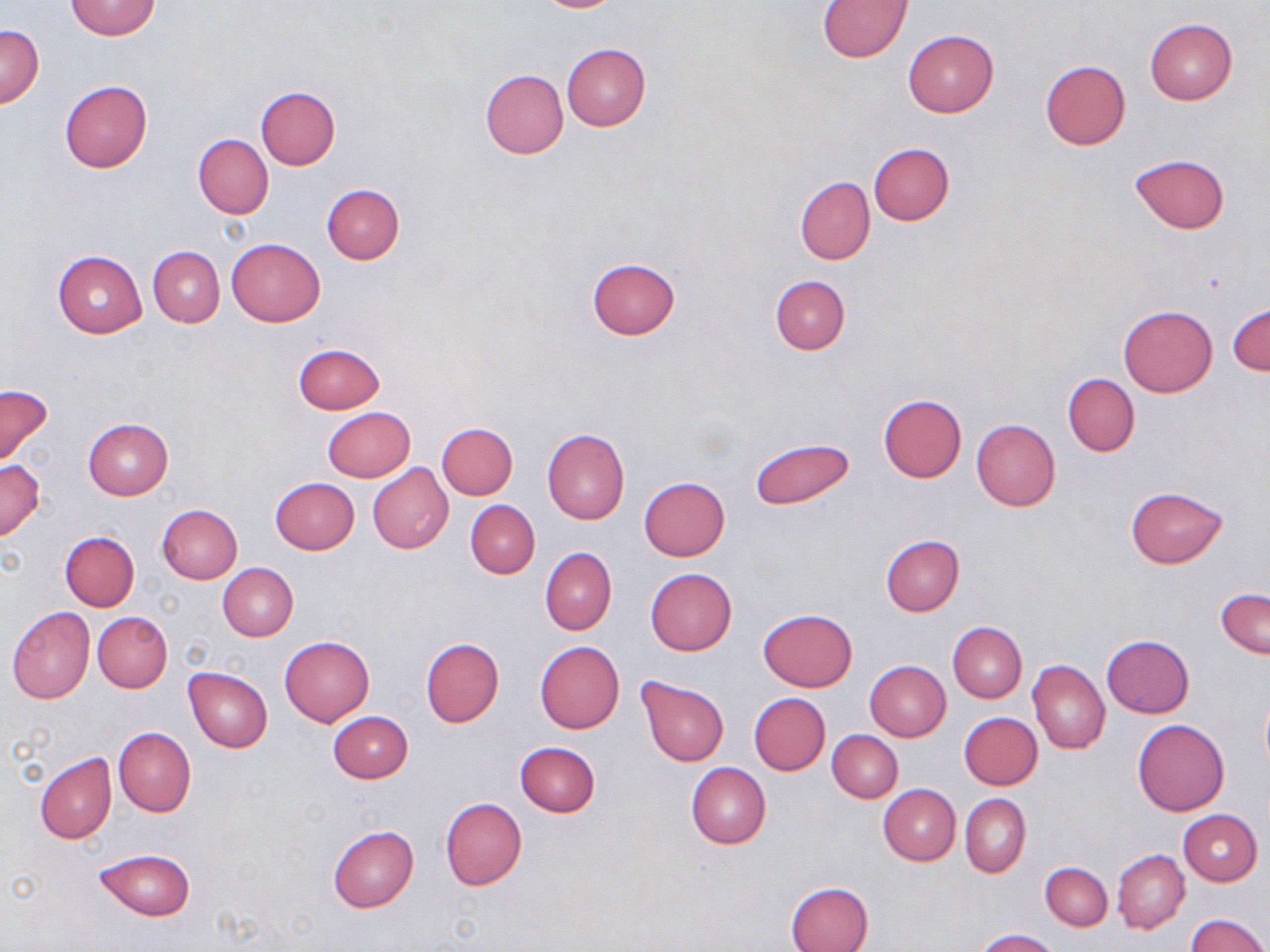
Summary:
  - Coordinate format: approximate bounding boxes as named x1/y1/x2/y2 corners in pixels
  - Uninfected red blood cell locations: (x1=534, y1=0, x2=624, y2=12), (x1=66, y1=1, x2=160, y2=40), (x1=818, y1=1, x2=911, y2=61), (x1=1145, y1=18, x2=1237, y2=105), (x1=0, y1=25, x2=44, y2=108), (x1=903, y1=30, x2=998, y2=117), (x1=561, y1=44, x2=651, y2=131), (x1=1039, y1=60, x2=1130, y2=150), (x1=480, y1=69, x2=568, y2=159), (x1=59, y1=81, x2=153, y2=171), (x1=256, y1=86, x2=340, y2=169), (x1=193, y1=134, x2=273, y2=218), (x1=867, y1=143, x2=954, y2=225), (x1=1130, y1=154, x2=1229, y2=235), (x1=795, y1=177, x2=874, y2=264), (x1=322, y1=184, x2=404, y2=263), (x1=227, y1=237, x2=325, y2=326), (x1=148, y1=246, x2=224, y2=327), (x1=52, y1=250, x2=146, y2=339), (x1=587, y1=257, x2=680, y2=339), (x1=770, y1=275, x2=850, y2=354), (x1=1228, y1=303, x2=1269, y2=375), (x1=1119, y1=305, x2=1217, y2=397), (x1=293, y1=343, x2=385, y2=413), (x1=1063, y1=374, x2=1139, y2=457), (x1=0, y1=384, x2=54, y2=469), (x1=878, y1=395, x2=967, y2=483), (x1=323, y1=407, x2=415, y2=482), (x1=83, y1=418, x2=172, y2=499), (x1=972, y1=420, x2=1061, y2=511), (x1=437, y1=422, x2=517, y2=500), (x1=542, y1=428, x2=630, y2=524), (x1=750, y1=438, x2=855, y2=509), (x1=0, y1=459, x2=45, y2=542), (x1=368, y1=464, x2=453, y2=554), (x1=270, y1=477, x2=359, y2=555), (x1=639, y1=477, x2=730, y2=560), (x1=1126, y1=487, x2=1228, y2=568), (x1=465, y1=499, x2=540, y2=578), (x1=156, y1=504, x2=242, y2=583), (x1=61, y1=531, x2=139, y2=611), (x1=881, y1=536, x2=964, y2=615), (x1=540, y1=548, x2=616, y2=634), (x1=218, y1=563, x2=297, y2=641), (x1=645, y1=568, x2=737, y2=655), (x1=1215, y1=587, x2=1270, y2=660), (x1=7, y1=607, x2=95, y2=704), (x1=759, y1=609, x2=857, y2=691), (x1=93, y1=612, x2=172, y2=692), (x1=947, y1=622, x2=1026, y2=702), (x1=1101, y1=635, x2=1193, y2=718), (x1=279, y1=636, x2=375, y2=727), (x1=421, y1=637, x2=505, y2=727), (x1=535, y1=640, x2=624, y2=733), (x1=1028, y1=659, x2=1110, y2=754), (x1=865, y1=661, x2=950, y2=742), (x1=183, y1=666, x2=273, y2=752), (x1=636, y1=677, x2=730, y2=767), (x1=1260, y1=691, x2=1270, y2=773), (x1=749, y1=692, x2=830, y2=776), (x1=328, y1=711, x2=413, y2=783), (x1=958, y1=713, x2=1043, y2=790), (x1=1132, y1=718, x2=1229, y2=816), (x1=113, y1=728, x2=196, y2=817), (x1=828, y1=729, x2=902, y2=802), (x1=515, y1=741, x2=600, y2=817), (x1=35, y1=753, x2=116, y2=843), (x1=686, y1=762, x2=771, y2=849), (x1=879, y1=785, x2=960, y2=865), (x1=960, y1=794, x2=1030, y2=876), (x1=439, y1=798, x2=526, y2=890), (x1=1178, y1=809, x2=1261, y2=885), (x1=328, y1=825, x2=419, y2=913), (x1=94, y1=849, x2=196, y2=920), (x1=1113, y1=849, x2=1189, y2=934), (x1=1039, y1=862, x2=1112, y2=931), (x1=787, y1=881, x2=873, y2=952), (x1=1186, y1=914, x2=1269, y2=952), (x1=977, y1=929, x2=1058, y2=951)
  - Slide-level diagnosis: no evidence of blood parasites
  - Magnification: 1000x
  - Modality: optical microscopy
  - Image size: 1270×952 pixels
  - Preparation: thin blood film
  - Stain: May-Grünwald-Giemsa
  - Field of view: single